State which parasite is depicted.
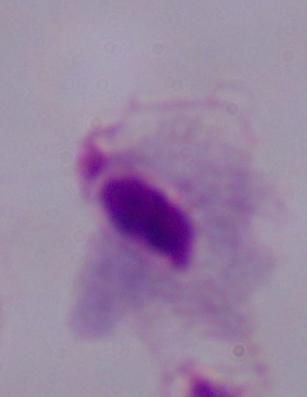

A trichomonad.

modality = micrograph
magnification = 1000x